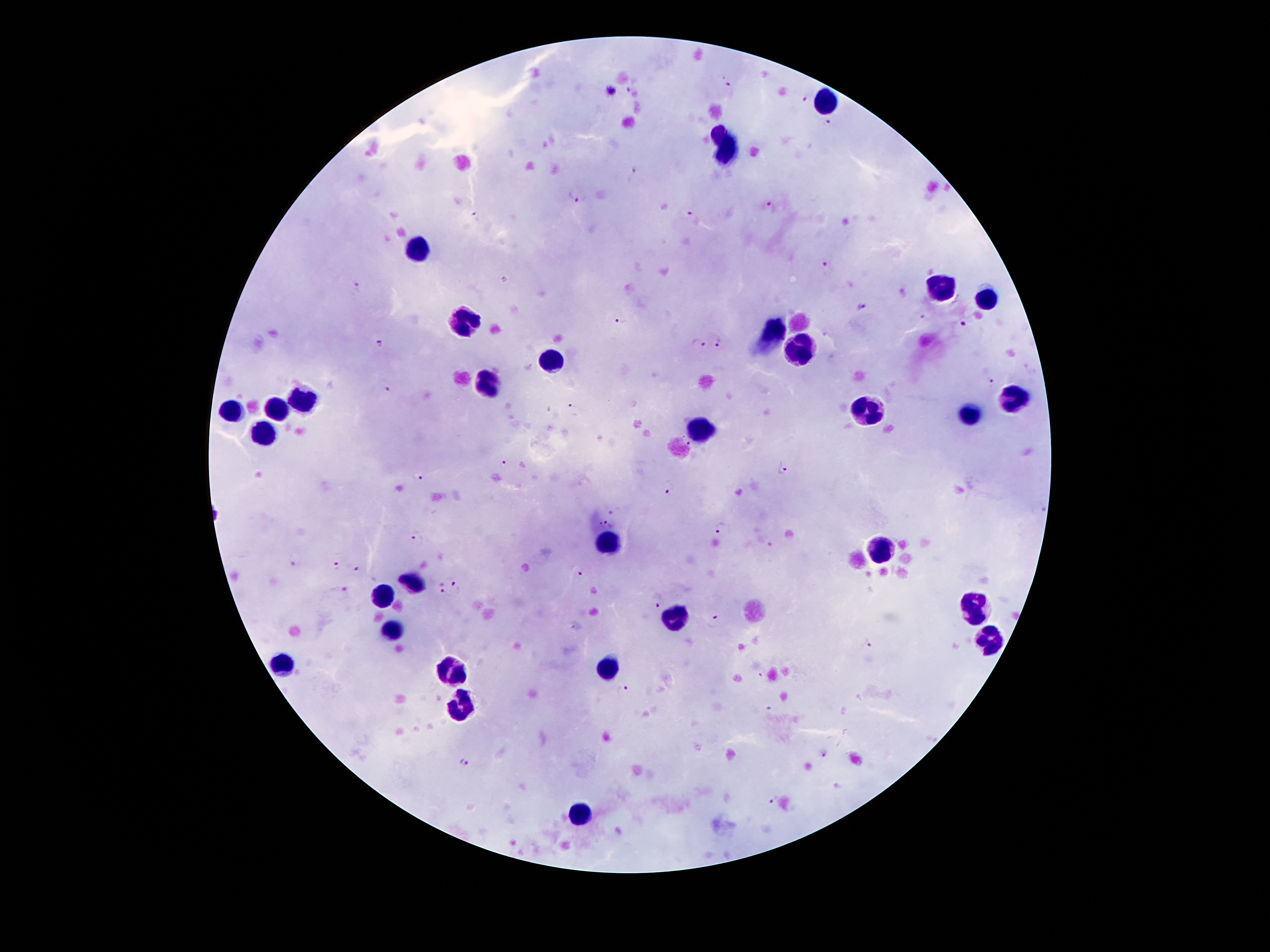
Approximate object centers, in pixels from the top-left corner. Leukocyte locations: (x=824, y=98), (x=720, y=132), (x=728, y=151), (x=421, y=252), (x=944, y=289), (x=986, y=301), (x=462, y=322), (x=771, y=335), (x=801, y=350), (x=554, y=361), (x=487, y=387), (x=303, y=398), (x=1014, y=399), (x=277, y=408), (x=866, y=411), (x=232, y=412), (x=970, y=414), (x=701, y=428), (x=265, y=430), (x=601, y=544), (x=878, y=552), (x=415, y=583), (x=384, y=594), (x=976, y=605), (x=672, y=618), (x=394, y=631), (x=991, y=639), (x=282, y=664), (x=606, y=669), (x=449, y=672), (x=462, y=704), (x=580, y=814). Plasmodium parasite locations: (x=730, y=81), (x=629, y=90), (x=805, y=100), (x=829, y=122), (x=634, y=169), (x=574, y=195), (x=773, y=204), (x=691, y=215), (x=474, y=217), (x=825, y=266), (x=357, y=286), (x=862, y=307), (x=924, y=317), (x=623, y=319), (x=961, y=324), (x=717, y=340), (x=697, y=343), (x=380, y=344), (x=992, y=380), (x=387, y=389), (x=573, y=407), (x=689, y=444), (x=506, y=463), (x=784, y=468), (x=422, y=477), (x=669, y=491), (x=607, y=521), (x=721, y=527), (x=417, y=538), (x=769, y=545), (x=293, y=561), (x=334, y=564), (x=355, y=569), (x=581, y=574), (x=456, y=585), (x=344, y=589), (x=441, y=593), (x=657, y=602), (x=717, y=617), (x=867, y=645), (x=625, y=689), (x=770, y=711), (x=826, y=756), (x=466, y=760), (x=774, y=800). Smartphone photograph taken through the microscope eyepiece. One field from this slide. Giemsa-stained preparation. 100x magnification. Patient malaria status: positive for Plasmodium falciparum. Thick peripheral-blood smear. Image is 1270×952 pixels.